Classify this cell by malaria status.
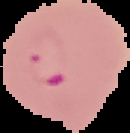
Parasitized.

Summary:
  - Preparation: thin blood smear
  - Image size: 130×133 pixels
  - Image type: cell region segmented out of the field of view; surrounding area masked to black